Outline each blood parasite and name the species.
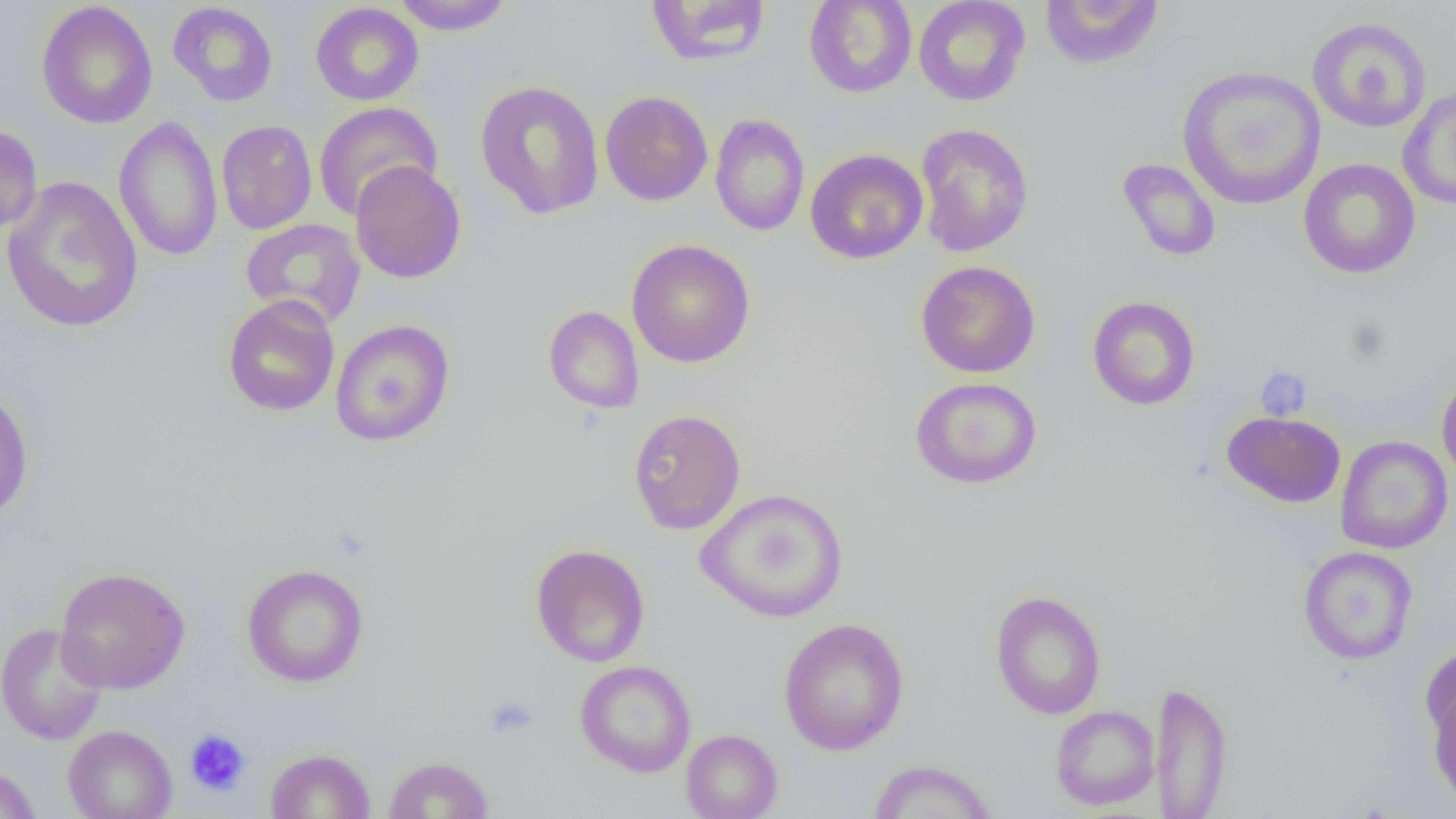

No blood parasites seen.

Summary:
  - Coordinate format: approximate bounding boxes as named x1/y1/x2/y2 corners in pixels
  - Platelet locations: (x1=1254, y1=367, x2=1312, y2=421), (x1=485, y1=696, x2=538, y2=738), (x1=184, y1=728, x2=252, y2=797)
  - Uninfected red blood cell locations: (x1=390, y1=0, x2=515, y2=36), (x1=803, y1=0, x2=918, y2=98), (x1=913, y1=0, x2=1031, y2=106), (x1=1039, y1=0, x2=1165, y2=71), (x1=36, y1=1, x2=158, y2=129), (x1=645, y1=1, x2=773, y2=67), (x1=167, y1=2, x2=279, y2=107), (x1=310, y1=2, x2=424, y2=106), (x1=1307, y1=16, x2=1432, y2=133), (x1=1177, y1=65, x2=1327, y2=211), (x1=475, y1=80, x2=605, y2=219), (x1=1398, y1=87, x2=1456, y2=210), (x1=600, y1=90, x2=713, y2=206), (x1=313, y1=102, x2=443, y2=221), (x1=710, y1=113, x2=809, y2=237), (x1=113, y1=115, x2=223, y2=261), (x1=216, y1=119, x2=317, y2=235), (x1=914, y1=123, x2=1034, y2=258), (x1=0, y1=125, x2=43, y2=235), (x1=805, y1=148, x2=928, y2=264), (x1=1116, y1=158, x2=1222, y2=262), (x1=1298, y1=158, x2=1421, y2=279), (x1=350, y1=160, x2=466, y2=284), (x1=2, y1=175, x2=143, y2=334), (x1=240, y1=218, x2=366, y2=328), (x1=627, y1=239, x2=756, y2=368), (x1=916, y1=261, x2=1041, y2=378), (x1=223, y1=294, x2=340, y2=417), (x1=1087, y1=296, x2=1201, y2=411), (x1=543, y1=305, x2=645, y2=414), (x1=330, y1=320, x2=455, y2=447), (x1=1436, y1=373, x2=1456, y2=488), (x1=910, y1=376, x2=1043, y2=490), (x1=0, y1=381, x2=34, y2=523), (x1=628, y1=408, x2=746, y2=535), (x1=1222, y1=411, x2=1346, y2=507), (x1=1335, y1=435, x2=1453, y2=554), (x1=695, y1=487, x2=848, y2=623), (x1=531, y1=544, x2=650, y2=667), (x1=1298, y1=546, x2=1418, y2=665), (x1=241, y1=563, x2=369, y2=687), (x1=55, y1=566, x2=191, y2=694), (x1=990, y1=590, x2=1106, y2=720), (x1=778, y1=617, x2=909, y2=756), (x1=0, y1=622, x2=109, y2=746), (x1=1420, y1=642, x2=1456, y2=746), (x1=575, y1=660, x2=696, y2=778), (x1=1153, y1=679, x2=1233, y2=818), (x1=1427, y1=686, x2=1456, y2=807), (x1=1050, y1=705, x2=1159, y2=810), (x1=63, y1=724, x2=177, y2=819), (x1=681, y1=729, x2=783, y2=819), (x1=265, y1=748, x2=376, y2=819), (x1=383, y1=755, x2=494, y2=818), (x1=868, y1=759, x2=999, y2=819), (x1=0, y1=762, x2=42, y2=819)
  - Slide-level diagnosis: no evidence of blood parasites
  - Image size: 1456×819 pixels
  - Field of view: single
  - Preparation: thin blood film
  - Modality: light microscopy
  - Magnification: 1000x